Assess this cell for malaria.
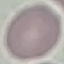

It is uninfected.

image type = cell patch, automatically extracted from a larger field of view and resized to 64 × 64 pixels
capture = smartphone camera at the microscope eyepiece
stain = Giemsa
preparation = thin smear